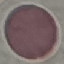
Result: no malaria parasites seen. Automatically extracted cell patch, resized to 64 × 64 pixels. Thin smear of blood. Giemsa-stained preparation. Photographed with a smartphone camera at the microscope eyepiece.